Locate every blood parasite and identify its species.
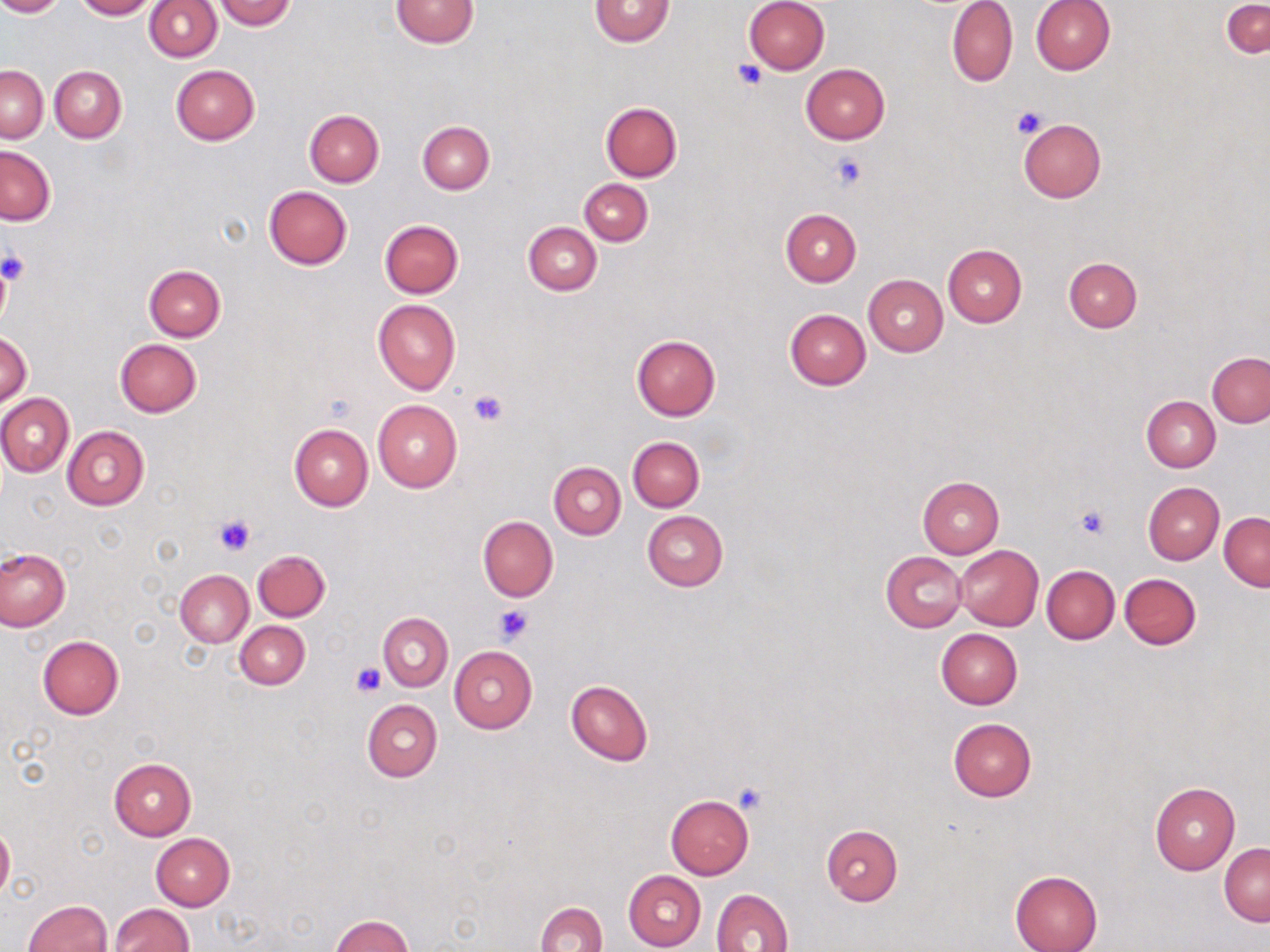
No blood parasites observed.

{
  "slide_level_diagnosis": "no evidence of blood parasites",
  "platelet_locations": "approximate bounding boxes as [x1, y1, x2, y2] in pixels: [732, 59, 768, 91], [1010, 106, 1048, 139], [830, 153, 866, 190], [0, 251, 29, 284], [467, 387, 509, 426], [1075, 505, 1111, 540], [212, 512, 257, 557], [493, 604, 532, 646], [352, 662, 385, 696], [732, 782, 769, 815]",
  "stain": "May-Grünwald-Giemsa",
  "field_of_view": "single",
  "modality": "optical microscopy",
  "uninfected_red_blood_cell_locations": "approximate bounding boxes as [x1, y1, x2, y2] in pixels: [1, 0, 63, 17], [73, 0, 157, 20], [213, 0, 297, 29], [390, 0, 479, 48], [589, 0, 673, 47], [743, 0, 830, 75], [946, 0, 1018, 87], [1030, 0, 1115, 75], [144, 1, 222, 62], [1223, 2, 1270, 57], [170, 64, 261, 145], [801, 64, 890, 144], [1, 65, 47, 142], [49, 65, 127, 142], [600, 100, 682, 181], [304, 110, 384, 187], [1019, 118, 1106, 202], [418, 120, 494, 194], [0, 145, 55, 225], [579, 178, 652, 245], [262, 185, 352, 270], [780, 209, 861, 286], [379, 219, 464, 299], [523, 221, 601, 295], [942, 244, 1028, 327], [1062, 257, 1143, 333], [144, 264, 226, 341], [863, 274, 948, 356], [372, 299, 460, 394], [784, 308, 871, 389], [1, 331, 32, 408], [631, 334, 721, 420], [115, 339, 202, 417], [1207, 351, 1270, 428], [0, 394, 74, 477], [1141, 395, 1219, 472], [372, 400, 461, 494], [289, 424, 372, 510], [62, 426, 149, 510], [627, 436, 704, 511], [548, 462, 625, 539], [917, 476, 1005, 557], [1143, 482, 1224, 565], [642, 511, 728, 591], [1219, 512, 1270, 591], [478, 515, 558, 602], [954, 545, 1044, 630], [0, 549, 70, 632], [253, 549, 330, 621], [881, 551, 965, 632], [1042, 565, 1119, 642], [175, 569, 253, 647], [1119, 573, 1201, 650], [379, 613, 452, 691], [235, 621, 310, 689], [936, 629, 1022, 710], [37, 636, 124, 720], [449, 646, 537, 733], [565, 680, 653, 766], [362, 699, 442, 782], [948, 717, 1036, 801], [108, 757, 197, 841], [1149, 781, 1238, 876], [666, 795, 754, 879], [0, 824, 14, 899], [820, 824, 903, 906], [151, 833, 234, 909], [1219, 843, 1269, 925], [1010, 869, 1103, 952], [624, 870, 706, 950], [710, 889, 793, 952], [23, 900, 112, 952], [535, 901, 608, 952], [108, 903, 194, 952], [330, 915, 415, 952]",
  "magnification": "1000x",
  "image_size": "1270×952 pixels",
  "preparation": "thin blood smear"
}